Locate and identify every blood parasite.
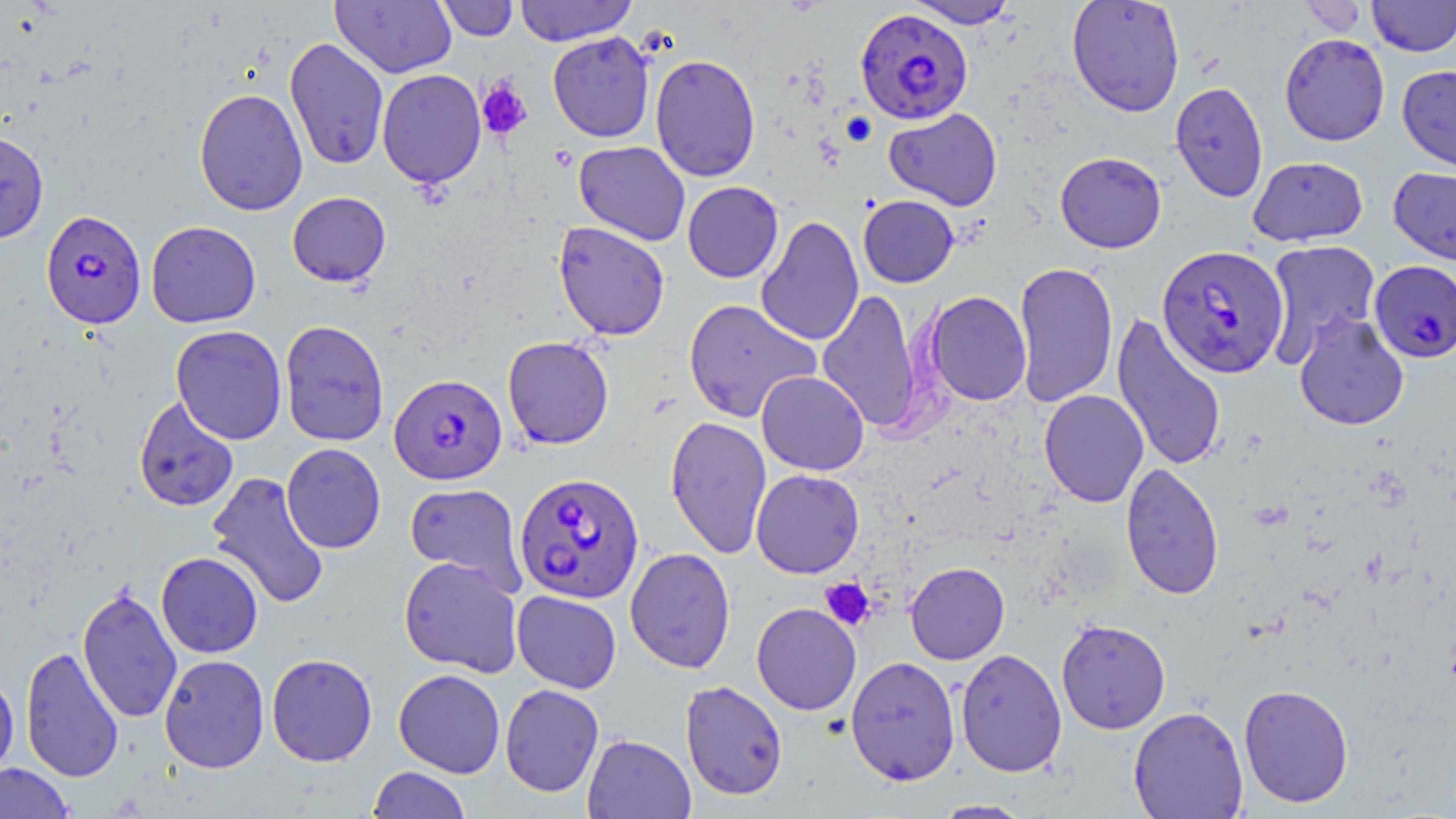

Approximate bounding boxes as [x1, y1, x2, y2] in pixels.
Plasmodium falciparum-infected red blood cells: [855, 8, 973, 125], [41, 209, 146, 329], [1156, 244, 1289, 378], [1369, 260, 1456, 364], [389, 373, 507, 485], [513, 472, 644, 605].
No Plasmodium ovale, Plasmodium malariae, Plasmodium vivax, Babesia divergens, or Trypanosoma brucei observed.

Platelet locations: [476, 78, 532, 139], [820, 578, 874, 631]. Uninfected red blood cell locations: [331, 0, 456, 78], [435, 0, 520, 41], [514, 0, 637, 45], [905, 0, 1020, 29], [1066, 0, 1185, 117], [1367, 0, 1456, 57], [1301, 1, 1367, 38], [548, 32, 655, 143], [1279, 33, 1390, 146], [284, 37, 389, 171], [649, 53, 761, 182], [1396, 65, 1456, 172], [376, 69, 486, 189], [1170, 81, 1269, 202], [193, 88, 308, 216], [883, 107, 1003, 211], [0, 131, 49, 243], [573, 141, 690, 246], [1055, 151, 1166, 253], [1247, 156, 1368, 247], [1388, 166, 1456, 265], [682, 181, 783, 283], [287, 192, 391, 287], [858, 195, 959, 288], [755, 215, 864, 347], [146, 221, 261, 328], [553, 222, 670, 340], [1263, 240, 1382, 364], [1013, 260, 1118, 409], [817, 289, 924, 432], [924, 291, 1031, 406], [682, 298, 820, 423], [1111, 313, 1227, 474], [1294, 313, 1409, 431], [279, 320, 389, 446], [171, 325, 287, 444], [502, 336, 614, 449], [756, 371, 869, 475], [1039, 389, 1149, 507], [133, 395, 239, 512], [664, 415, 772, 559], [281, 443, 386, 553], [1120, 462, 1224, 600], [751, 468, 865, 578], [206, 471, 330, 610], [405, 482, 527, 594], [625, 547, 736, 673], [156, 552, 263, 658], [398, 556, 523, 677], [905, 561, 1010, 664], [77, 585, 183, 724], [512, 590, 622, 693], [751, 602, 861, 715], [1056, 618, 1170, 734], [20, 646, 124, 783], [955, 648, 1067, 777], [266, 653, 378, 766], [159, 654, 269, 773], [845, 656, 961, 786], [394, 669, 505, 778], [0, 673, 19, 779], [680, 680, 788, 801], [499, 684, 604, 797], [1238, 684, 1354, 808], [1128, 706, 1248, 819], [582, 734, 695, 819], [0, 762, 74, 819], [368, 767, 471, 819], [930, 799, 1035, 818]. Slide-level diagnosis: Plasmodium falciparum. May-Grünwald-Giemsa-stained preparation. 1000x magnification. Single field of view. Thin blood film. Optical microscopy. Image is 1456×819 pixels.